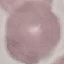

result = no malaria parasites detected
stain = Giemsa
capture = smartphone camera at the microscope eyepiece
preparation = thin blood smear
image type = automatically extracted cell patch, resized to 64 × 64 pixels